Assess the morphology of the red blood cells.
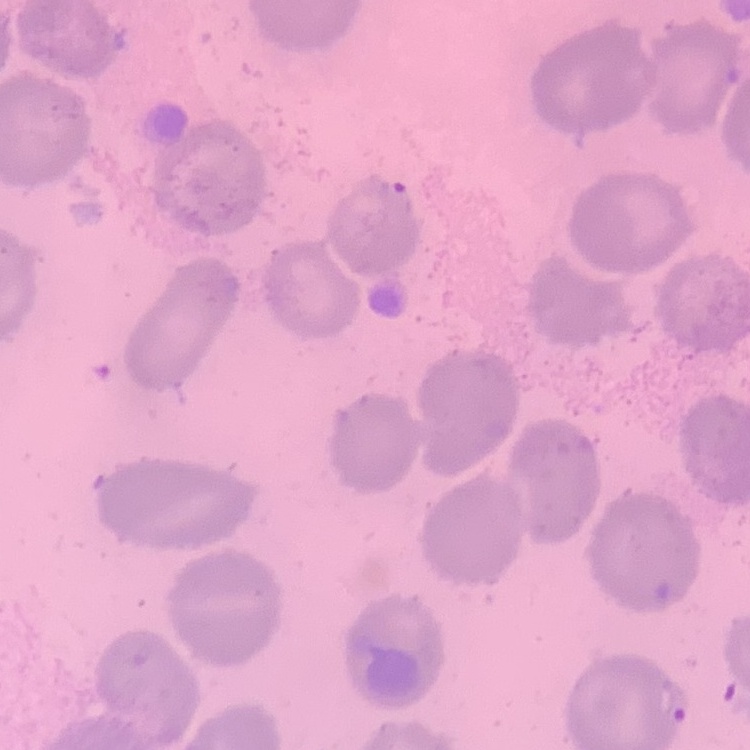

No rouleaux formation.

One tile cut from a larger photomicrograph. Field's or Giemsa stain. Thin blood smear.